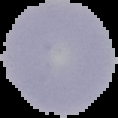

From a thin blood smear. Image is 118×118 pixels. Segmented cell region on a black background. Malaria status: uninfected.